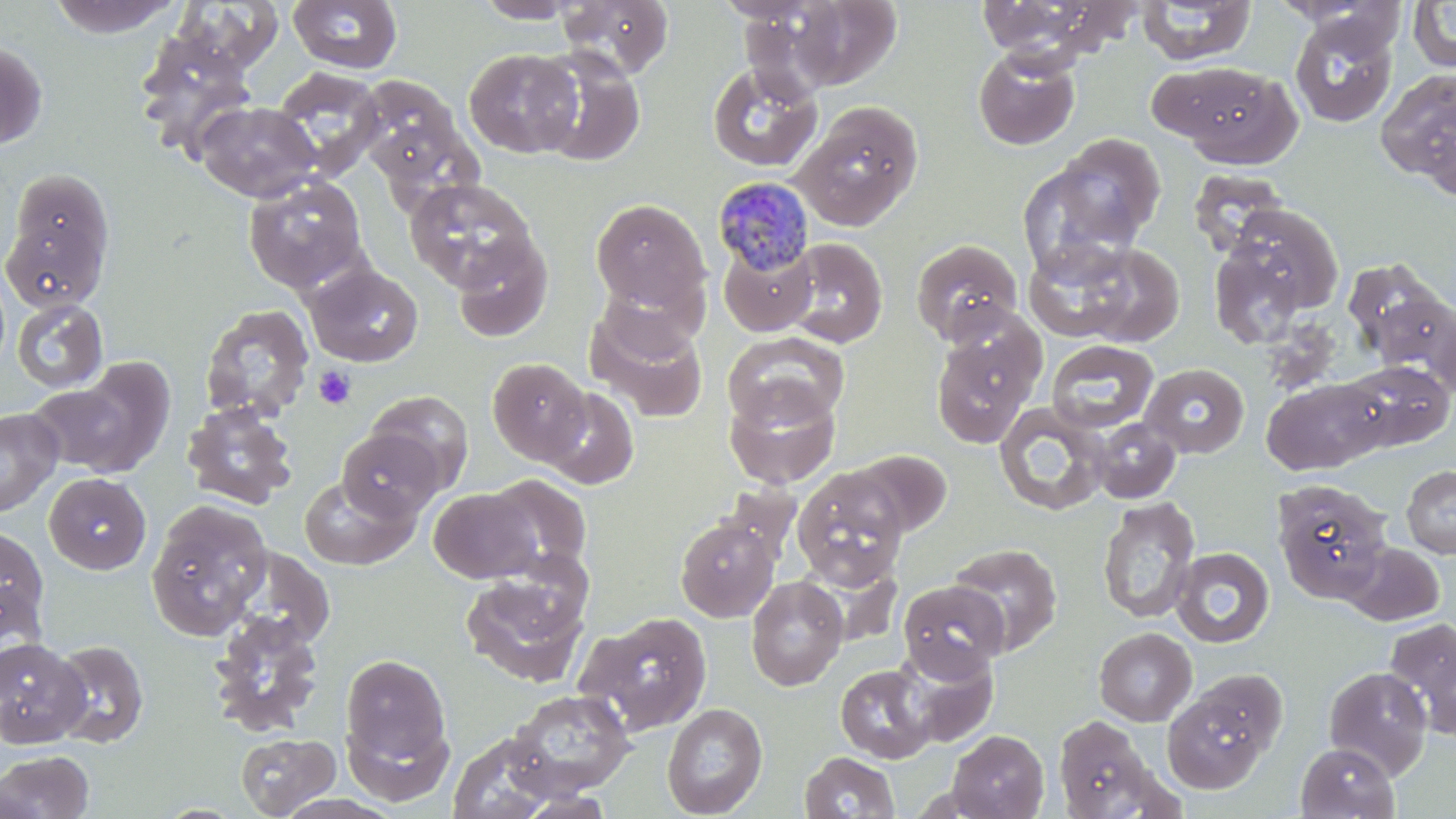

{
  "slide_level_diagnosis": "Plasmodium malariae",
  "modality": "light microscopy",
  "image_size": "1456×819 pixels",
  "preparation": "thin blood film",
  "stain": "May-Grünwald-Giemsa",
  "uninfected_red_blood_cell_locations": "approximate bounding boxes as (x1,y1)-(x2,y2) corner pairs in pixels: (47,0)-(183,38), (472,0)-(583,23), (558,0)-(675,79), (714,0)-(828,24), (779,0)-(903,91), (974,0)-(1121,64), (1136,0)-(1256,65), (1271,0)-(1398,33), (172,1)-(289,75), (287,1)-(403,74), (1407,1)-(1456,73), (1287,13)-(1399,128), (134,34)-(258,165), (0,41)-(47,149), (531,47)-(646,165), (973,47)-(1080,150), (464,48)-(582,158), (707,61)-(822,172), (1163,62)-(1302,166), (272,67)-(385,178), (1376,69)-(1456,189), (356,74)-(471,186), (794,100)-(924,231), (196,102)-(321,202), (1052,133)-(1167,247), (1015,160)-(1143,281), (10,169)-(113,270), (1190,170)-(1291,257), (243,173)-(369,294), (405,178)-(539,292), (590,198)-(710,316), (1219,203)-(1345,325), (1,215)-(107,311), (450,231)-(553,342), (784,237)-(888,348), (911,238)-(1023,344), (1022,238)-(1143,343), (719,241)-(817,336), (1067,241)-(1187,346), (303,262)-(424,366), (1368,285)-(1456,390), (11,298)-(108,393), (200,303)-(315,422), (1431,303)-(1456,399), (586,304)-(709,423), (929,321)-(1044,449), (723,331)-(850,431), (1046,339)-(1158,434), (42,356)-(176,479), (487,357)-(592,465), (1338,359)-(1454,452), (1141,363)-(1250,457), (1262,377)-(1388,475), (724,381)-(840,489), (541,386)-(639,489), (364,391)-(474,494), (182,401)-(297,509), (993,402)-(1111,516), (0,408)-(62,517), (1089,418)-(1182,503), (337,427)-(443,520), (845,449)-(952,538), (1401,464)-(1456,558), (792,468)-(910,588), (45,472)-(151,574), (299,474)-(419,570), (483,474)-(592,575), (1273,477)-(1395,604), (429,487)-(543,583), (1097,496)-(1201,624), (146,499)-(272,640), (675,517)-(780,621), (0,525)-(50,634), (1341,541)-(1444,626), (947,542)-(1063,654), (1170,546)-(1275,648), (459,565)-(591,688), (746,576)-(848,690), (0,577)-(48,687), (898,579)-(1009,679), (208,611)-(326,738), (575,611)-(712,736), (1384,617)-(1456,738), (1093,627)-(1198,726), (0,638)-(91,748), (47,639)-(149,748), (893,645)-(999,747), (340,651)-(453,789), (835,664)-(936,763), (1324,665)-(1433,778), (1161,682)-(1277,793), (507,689)-(636,796), (661,702)-(768,817), (1053,714)-(1159,819), (449,730)-(564,819), (947,730)-(1050,819), (236,732)-(340,818), (1295,742)-(1400,819), (0,750)-(94,818), (799,751)-(901,819)",
  "magnification": "1000x",
  "platelet_locations": "approximate bounding boxes as (x1,y1)-(x2,y2) corner pairs in pixels: (313,365)-(356,409)",
  "field_of_view": "single",
  "plasmodium_malariae_infected_red_blood_cell_locations": "approximate bounding boxes as (x1,y1)-(x2,y2) corner pairs in pixels: (712,176)-(814,276)"
}